Comment on the morphology of the red blood cells.
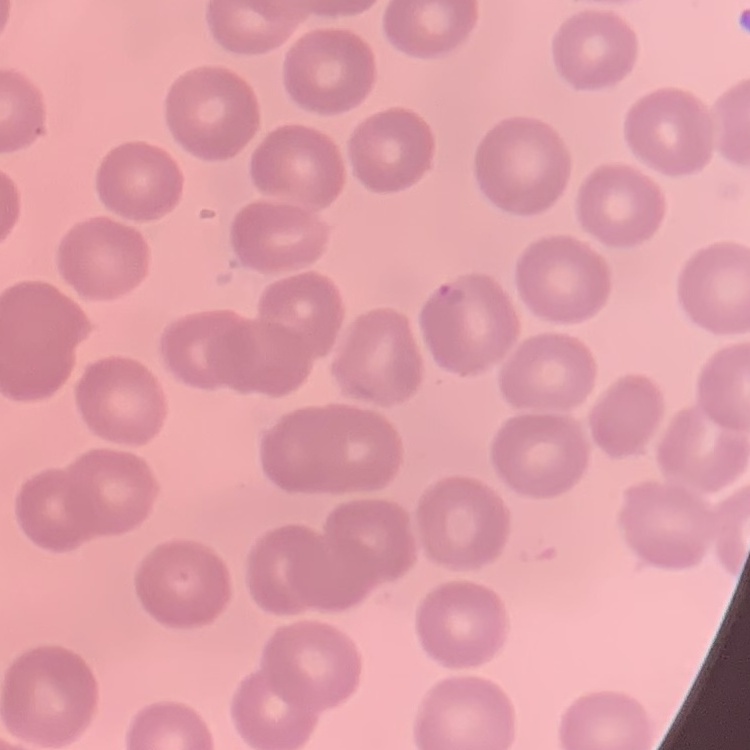

They show no rouleaux formation.

Stained with either Field's or Giemsa. Thin peripheral smear. Square crop of a larger photomicrograph.